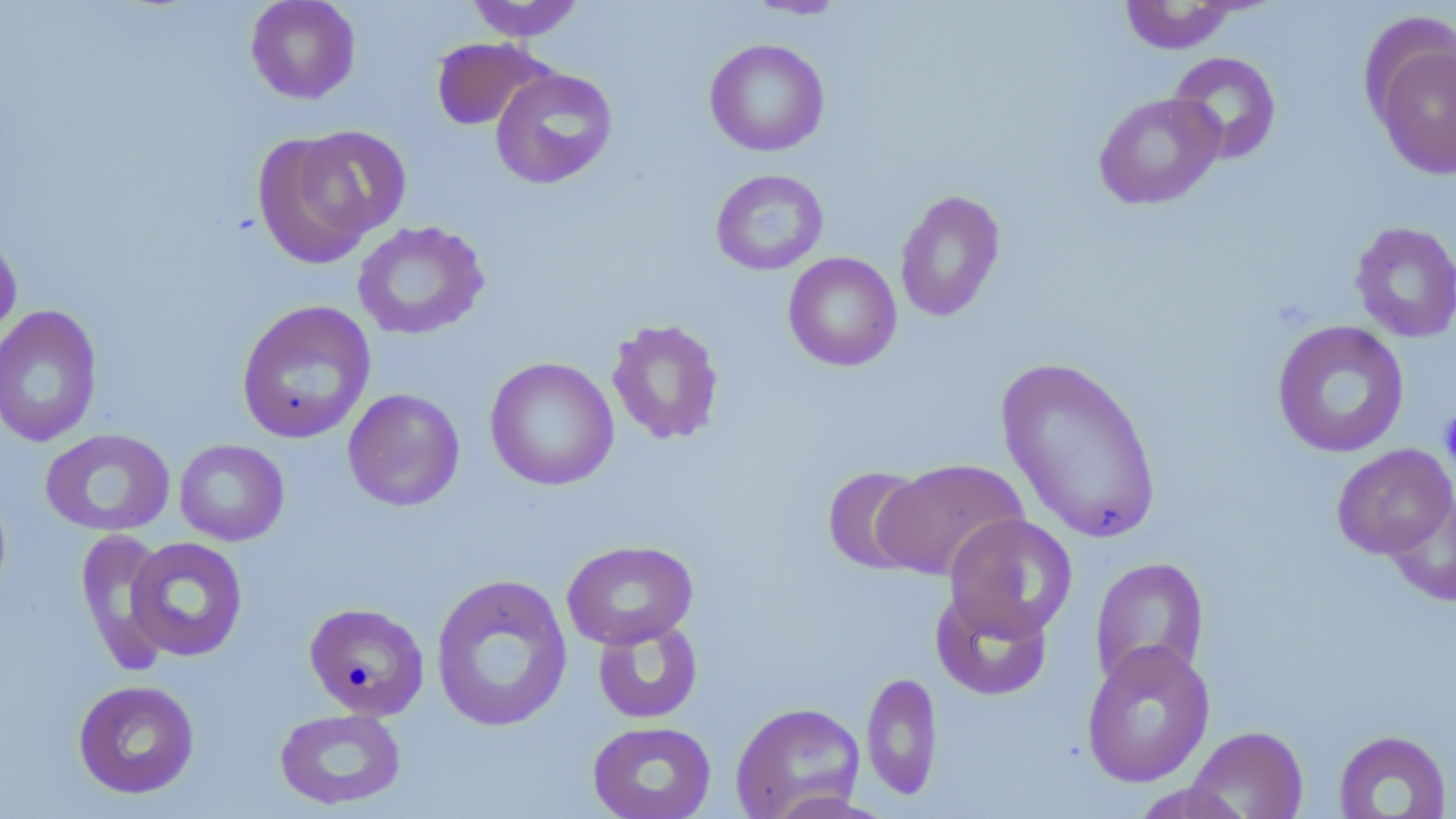

Summary:
  - Coordinate format: approximate bounding boxes as (x1,y1)-(x2,y2) corner pairs in pixels
  - Uninfected red blood cell locations: (245,0)-(361,105), (463,0)-(587,41), (741,0)-(850,20), (1117,1)-(1242,54), (1366,29)-(1456,180), (431,37)-(553,132), (704,39)-(830,157), (1166,51)-(1282,164), (490,67)-(618,189), (1093,92)-(1225,210), (295,125)-(412,239), (252,132)-(376,270), (710,169)-(829,276), (894,189)-(1006,322), (352,221)-(490,340), (1349,221)-(1456,342), (0,227)-(22,348), (783,252)-(902,371), (236,300)-(376,444), (0,305)-(103,447), (606,318)-(725,446), (1271,320)-(1410,458), (996,355)-(1163,545), (485,357)-(619,491), (342,388)-(466,512), (40,428)-(176,538), (174,439)-(289,546), (1331,444)-(1456,560), (875,458)-(1028,581), (821,465)-(933,576), (1385,490)-(1455,608), (943,513)-(1079,641), (76,529)-(174,673), (124,537)-(249,662), (561,539)-(699,650), (1089,555)-(1210,689), (430,572)-(573,733), (930,587)-(1053,700), (304,601)-(429,720), (592,616)-(704,724), (1081,640)-(1215,788), (861,670)-(943,801), (72,679)-(200,799), (730,702)-(866,819), (274,707)-(407,811), (587,720)-(717,819), (1184,725)-(1309,819), (1332,729)-(1453,818), (1126,781)-(1250,818)
  - Platelet locations: (1439,407)-(1456,473)
  - Slide-level diagnosis: negative for blood parasites
  - Modality: optical microscopy
  - Stain: May-Grünwald-Giemsa
  - Field of view: one of a larger specimen
  - Magnification: 1000x
  - Preparation: thin blood smear
  - Image size: 1456×819 pixels